Classify this cell by malaria status.
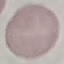
It is uninfected.

Automatically extracted cell patch, resized to 64 × 64 pixels. Photographed with a smartphone camera at the microscope eyepiece. Thin blood smear. Giemsa-stained preparation.